Comment on the morphology of the red blood cells.
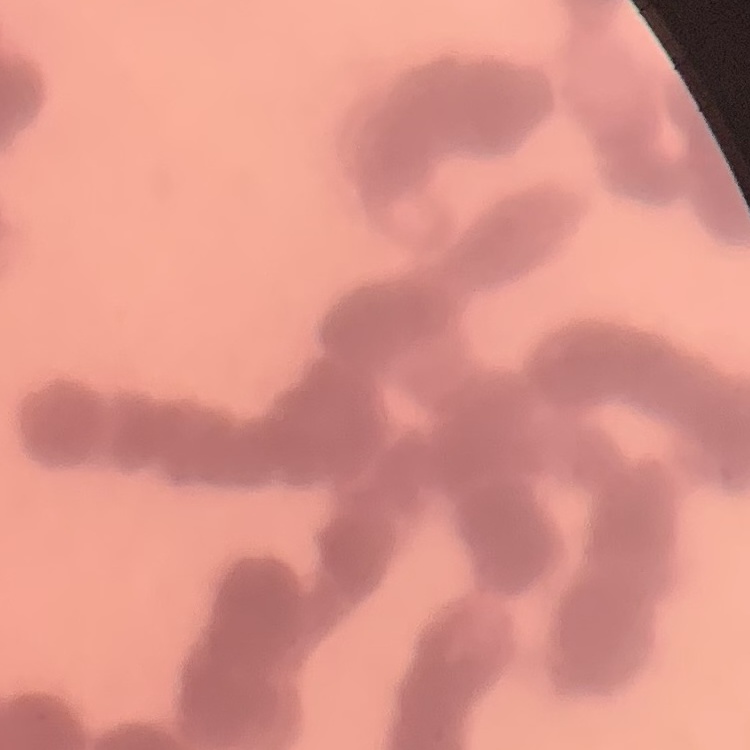
Rouleaux formation.

Summary:
  - Image type: one tile cut from a larger photomicrograph
  - Stain: Field's or Giemsa
  - Preparation: thin peripheral smear